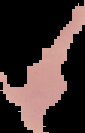
Summary:
  - Result: negative for malaria parasites
  - Image size: 85×133 pixels
  - Preparation: thin blood film
  - Image type: cell region segmented out of the field of view; surrounding area masked to black